Give the position of every Plasmodium parasite.
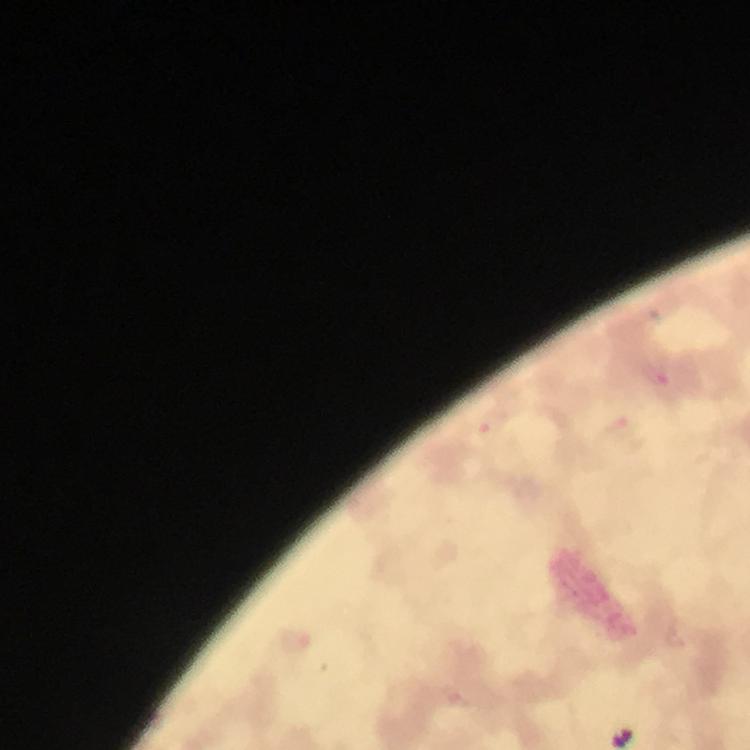

Approximate centers as (x, y) in pixels.
Plasmodium parasites: (658, 374), (619, 424), (485, 429), (295, 640).

Smartphone photograph taken through a microscope. A crop from one field of view. Image is 750×750 pixels. Giemsa-stained preparation. From a malaria diagnostic workup. Thick smear. Immersion oil was used. 100x magnification.